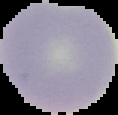

Summary:
  - Image type: cell region segmented out of the field of view; surrounding area masked to black
  - Preparation: thin blood film
  - Result: no malaria parasites seen
  - Image size: 118×115 pixels